Classify this cell by malaria status.
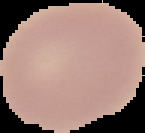
It is uninfected.

image_size: 145×133 pixels
image_type: segmented cell region on a black background
preparation: thin blood film